Identify the parasite.
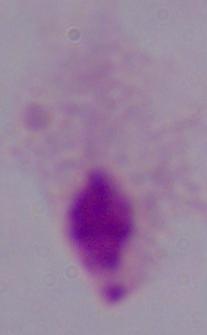
A trichomonad.

Summary:
  - Magnification: 1000x
  - Modality: photomicrograph